Assess this cell for malaria.
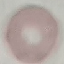
Uninfected.

{
  "preparation": "thin blood film",
  "stain": "Giemsa",
  "image_type": "automatically extracted cell patch, resized to 64 × 64 pixels",
  "capture": "smartphone through the microscope eyepiece"
}